Give the extent of all uninfected red blood cells.
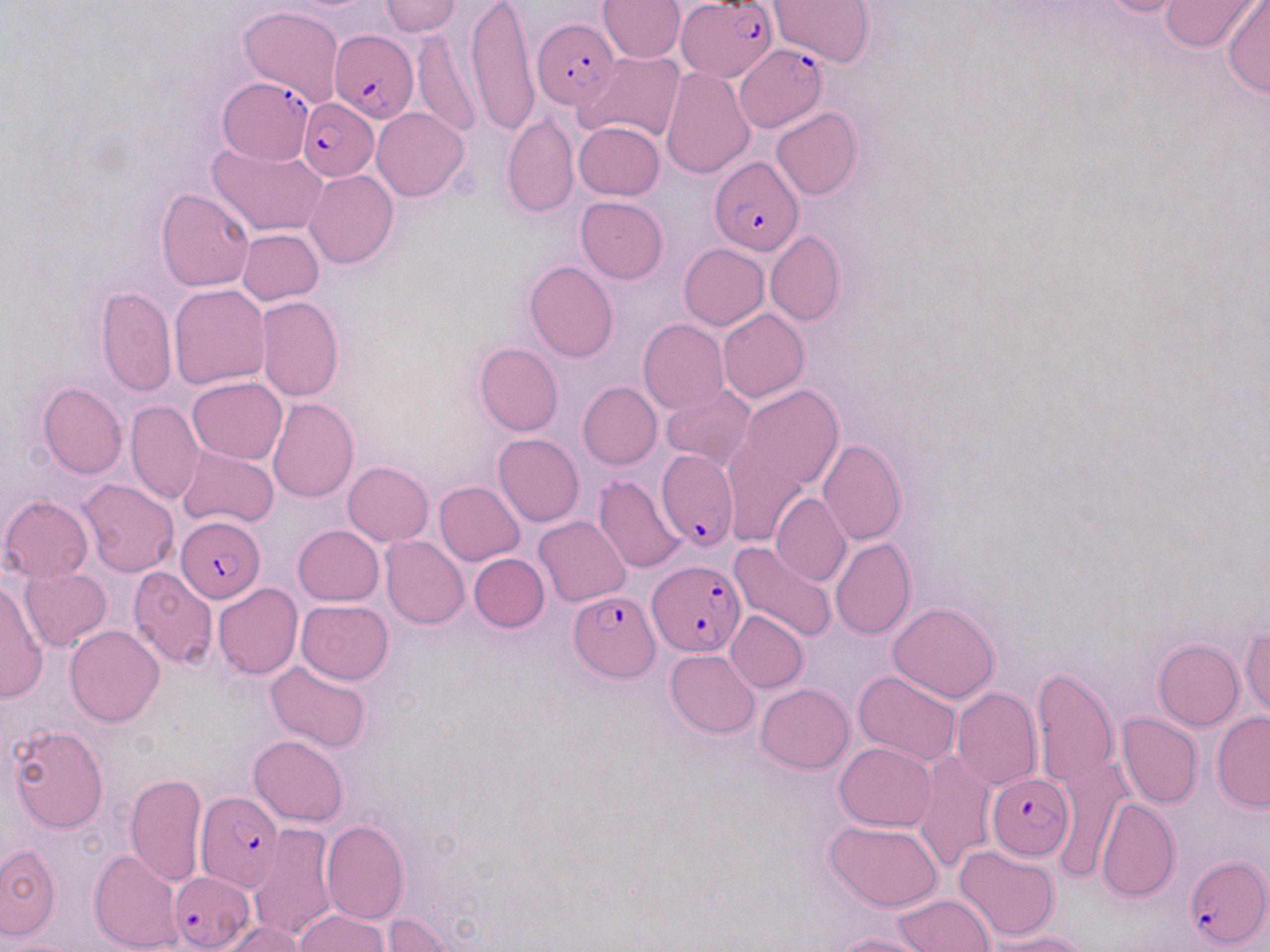

Approximate bounding boxes as named x1/y1/x2/y2 corners in pixels.
Uninfected red blood cells: (x1=378, y1=0, x2=461, y2=36), (x1=466, y1=0, x2=539, y2=136), (x1=769, y1=0, x2=873, y2=68), (x1=1089, y1=0, x2=1204, y2=19), (x1=1158, y1=0, x2=1270, y2=52), (x1=598, y1=1, x2=685, y2=63), (x1=1223, y1=3, x2=1269, y2=99), (x1=239, y1=6, x2=345, y2=108), (x1=411, y1=28, x2=480, y2=138), (x1=575, y1=52, x2=685, y2=142), (x1=660, y1=67, x2=754, y2=178), (x1=372, y1=107, x2=469, y2=200), (x1=771, y1=107, x2=862, y2=200), (x1=502, y1=112, x2=579, y2=218), (x1=574, y1=120, x2=664, y2=199), (x1=209, y1=142, x2=327, y2=236), (x1=305, y1=169, x2=399, y2=269), (x1=157, y1=189, x2=255, y2=291), (x1=575, y1=196, x2=667, y2=283), (x1=237, y1=229, x2=324, y2=306), (x1=765, y1=230, x2=844, y2=326), (x1=679, y1=244, x2=769, y2=330), (x1=524, y1=261, x2=618, y2=362), (x1=169, y1=285, x2=268, y2=389), (x1=97, y1=286, x2=176, y2=397), (x1=256, y1=296, x2=345, y2=401), (x1=718, y1=309, x2=809, y2=402), (x1=638, y1=319, x2=729, y2=414), (x1=474, y1=342, x2=563, y2=436), (x1=187, y1=377, x2=287, y2=464), (x1=38, y1=381, x2=127, y2=480), (x1=578, y1=382, x2=662, y2=469), (x1=661, y1=385, x2=755, y2=471), (x1=740, y1=386, x2=844, y2=489), (x1=267, y1=397, x2=359, y2=502), (x1=126, y1=400, x2=203, y2=503), (x1=493, y1=433, x2=585, y2=526), (x1=721, y1=438, x2=808, y2=546), (x1=817, y1=439, x2=905, y2=544), (x1=179, y1=446, x2=278, y2=530), (x1=343, y1=462, x2=434, y2=545), (x1=593, y1=475, x2=687, y2=574), (x1=78, y1=480, x2=178, y2=576), (x1=434, y1=480, x2=525, y2=565), (x1=770, y1=493, x2=851, y2=588), (x1=1, y1=496, x2=94, y2=583), (x1=534, y1=516, x2=630, y2=606), (x1=292, y1=525, x2=384, y2=606), (x1=380, y1=536, x2=469, y2=629), (x1=830, y1=538, x2=916, y2=640), (x1=729, y1=542, x2=836, y2=643), (x1=469, y1=554, x2=549, y2=632), (x1=127, y1=565, x2=219, y2=669), (x1=20, y1=567, x2=112, y2=649), (x1=0, y1=579, x2=48, y2=703), (x1=213, y1=583, x2=303, y2=679), (x1=296, y1=599, x2=394, y2=685), (x1=888, y1=601, x2=1000, y2=704), (x1=725, y1=610, x2=808, y2=693), (x1=65, y1=625, x2=165, y2=726), (x1=1240, y1=627, x2=1269, y2=718), (x1=1153, y1=638, x2=1243, y2=731), (x1=665, y1=649, x2=760, y2=738), (x1=264, y1=661, x2=372, y2=753), (x1=1031, y1=667, x2=1119, y2=789), (x1=854, y1=671, x2=963, y2=768), (x1=755, y1=683, x2=854, y2=772), (x1=952, y1=687, x2=1041, y2=790), (x1=1212, y1=711, x2=1270, y2=812), (x1=1117, y1=713, x2=1203, y2=808), (x1=7, y1=726, x2=109, y2=833), (x1=248, y1=735, x2=349, y2=826), (x1=835, y1=742, x2=935, y2=832), (x1=913, y1=749, x2=998, y2=873), (x1=1052, y1=755, x2=1132, y2=884), (x1=125, y1=774, x2=207, y2=886), (x1=1094, y1=798, x2=1180, y2=902), (x1=320, y1=819, x2=410, y2=925), (x1=824, y1=819, x2=944, y2=912), (x1=248, y1=824, x2=338, y2=942), (x1=0, y1=844, x2=60, y2=940), (x1=954, y1=845, x2=1060, y2=941), (x1=89, y1=849, x2=185, y2=951), (x1=894, y1=895, x2=995, y2=951), (x1=294, y1=910, x2=391, y2=952), (x1=384, y1=913, x2=461, y2=952), (x1=222, y1=920, x2=306, y2=952), (x1=986, y1=932, x2=1093, y2=952), (x1=830, y1=934, x2=933, y2=952).

Plasmodium falciparum-infected red blood cell locations: (x1=680, y1=1, x2=778, y2=79), (x1=534, y1=18, x2=619, y2=108), (x1=329, y1=29, x2=419, y2=122), (x1=734, y1=43, x2=828, y2=132), (x1=220, y1=79, x2=318, y2=167), (x1=299, y1=98, x2=379, y2=181), (x1=709, y1=155, x2=804, y2=256), (x1=655, y1=449, x2=736, y2=551), (x1=175, y1=517, x2=265, y2=602), (x1=648, y1=563, x2=745, y2=658), (x1=569, y1=590, x2=660, y2=682), (x1=987, y1=773, x2=1076, y2=861), (x1=195, y1=792, x2=284, y2=892), (x1=1183, y1=856, x2=1269, y2=950), (x1=170, y1=871, x2=254, y2=952). Slide-level diagnosis: Plasmodium falciparum. Image is 1270×952 pixels. Light microscopy. Thin blood film. 1000x magnification. Single field of view. May-Grünwald-Giemsa-stained preparation.